Point out each leukocyte.
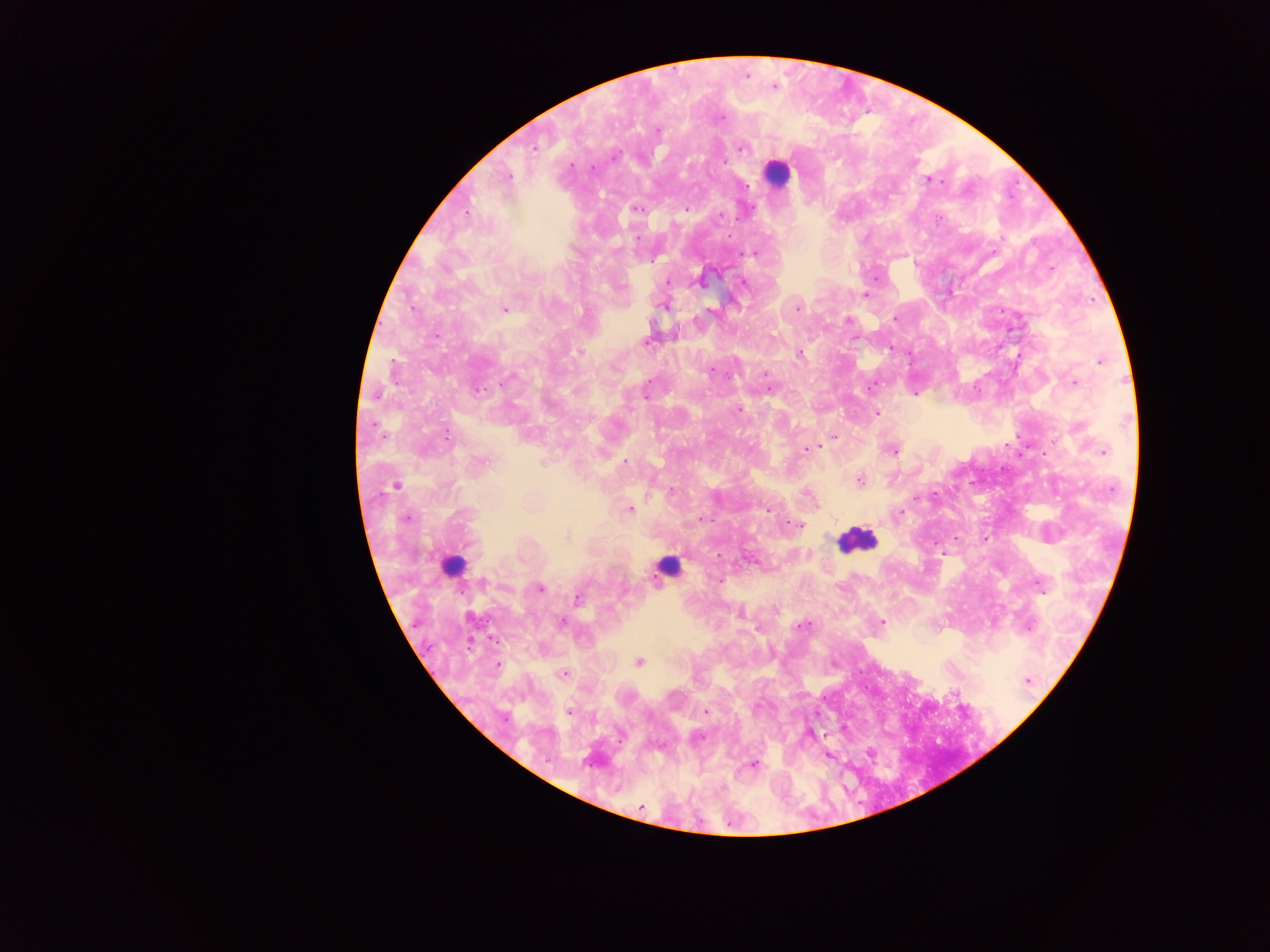

Approximate centers as x y in pixels.
Leukocytes: 776 173; 856 540; 452 562; 667 567.

Malaria parasite locations: 774 86; 657 130; 742 146; 533 147; 507 177; 929 180; 637 208; 686 209; 466 212; 719 217; 756 253; 1050 267; 876 277; 667 281; 742 282; 866 295; 665 304; 797 307; 503 309; 894 318; 848 320; 647 340; 580 351; 798 354; 1100 360; 1074 382; 872 385; 914 393; 738 409; 876 412; 446 435; 833 438; 820 446; 807 449; 891 449; 1104 451; 480 462; 544 462; 859 480; 397 485; 932 495; 629 509; 766 509; 898 512; 406 517; 701 518; 799 526; 985 538; 941 552; 719 580; 1039 585; 540 588; 578 598; 775 608; 740 613; 561 622; 881 622; 802 626; 757 629; 638 661; 563 674; 1026 680; 953 692; 569 711; 705 711; 810 734; 696 737; 869 753; 827 754; 753 764. Collected in Ghana. Thick blood film. Single field of view. Image is 1270×952 pixels. Photographed through a microscope with a mobile-phone camera.